Identify the parasite.
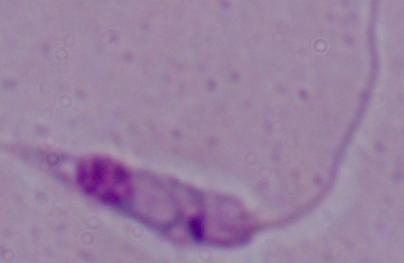
Leishmania.

Captured at 1000x magnification. Micrograph.